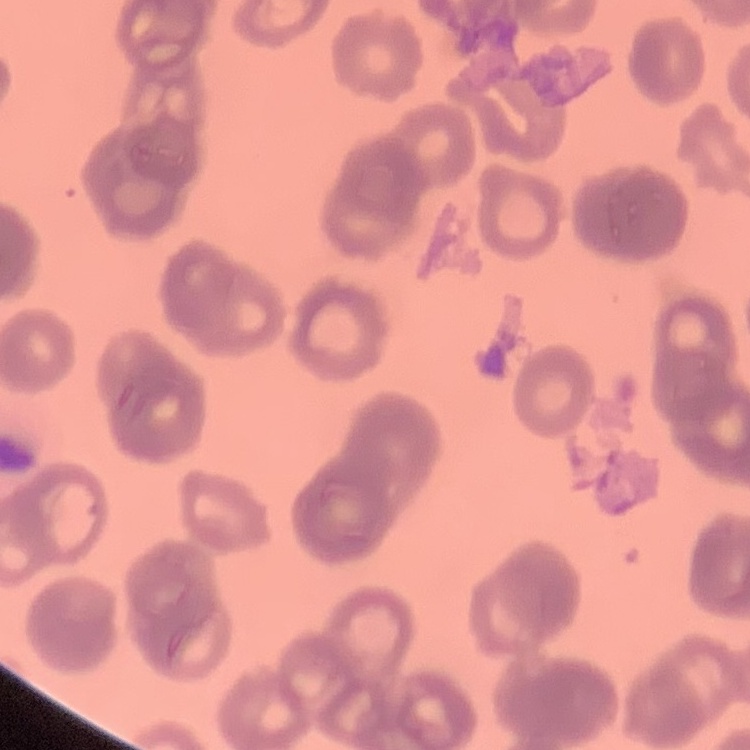

Summary:
  - Red blood cell morphology: rouleaux formation
  - Stain: Field's or Giemsa
  - Image type: one tile cut from a larger photomicrograph
  - Preparation: thin blood smear